Identify the cell.
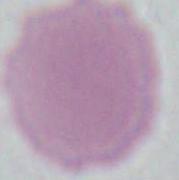

An erythrocyte.

Summary:
  - Magnification: 1000x
  - Modality: micrograph